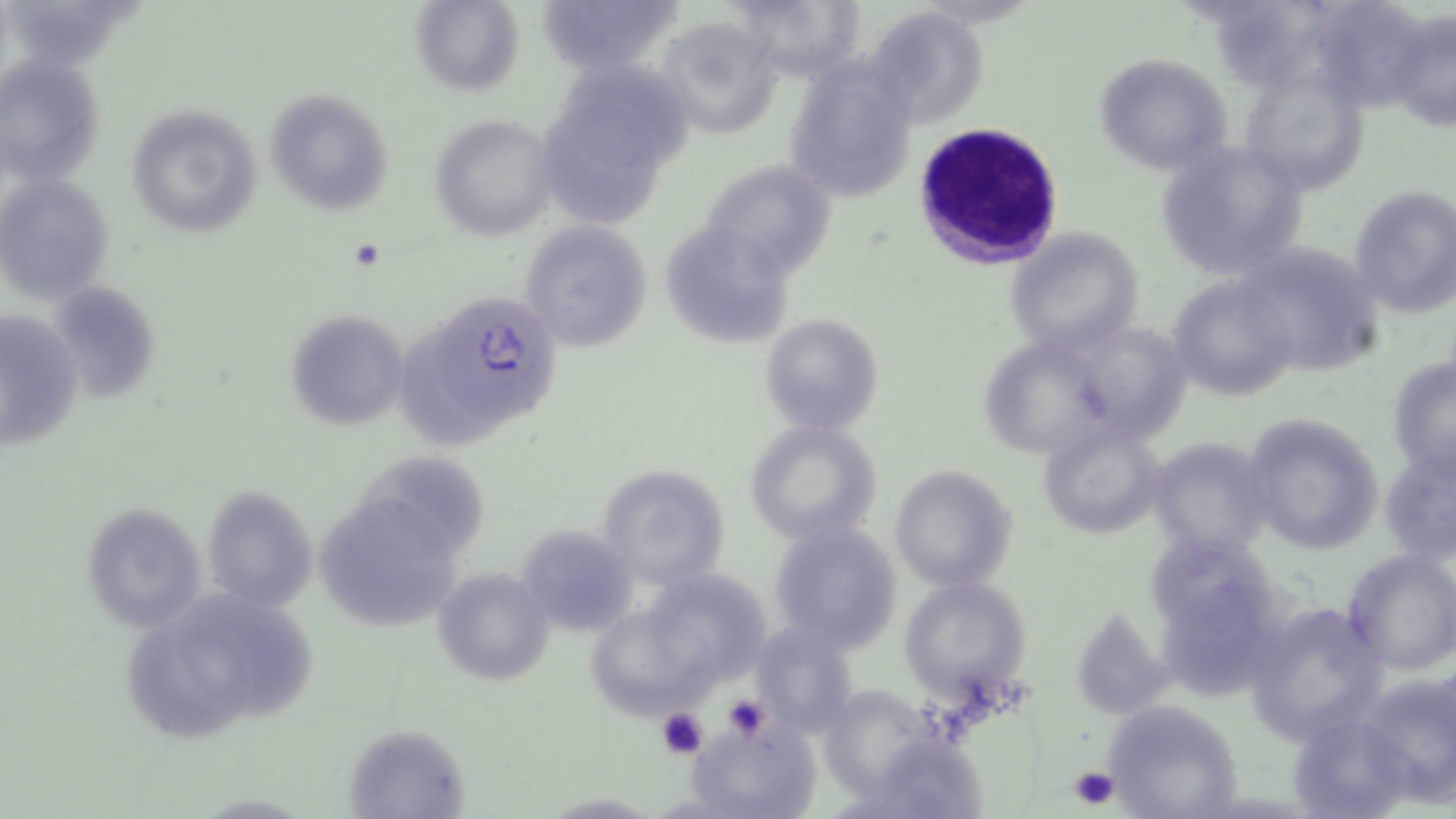
Approximate bounding boxes as (x1, y1, x2, y2) in pixels. Uninfected red blood cell locations: (408, 0, 524, 99), (724, 0, 866, 84), (533, 1, 681, 77), (1308, 1, 1435, 111), (866, 5, 989, 127), (1385, 13, 1456, 133), (655, 16, 782, 139), (1092, 52, 1235, 176), (0, 53, 107, 189), (782, 54, 920, 206), (574, 67, 694, 172), (1241, 67, 1370, 196), (262, 88, 397, 218), (125, 102, 262, 239), (562, 104, 664, 235), (429, 113, 560, 241), (1151, 140, 1311, 282), (697, 156, 839, 281), (1, 173, 116, 304), (1349, 184, 1456, 316), (517, 219, 655, 353), (1005, 225, 1145, 355), (666, 233, 812, 344), (1229, 242, 1384, 376), (1167, 272, 1300, 404), (47, 284, 159, 401), (1, 308, 83, 454), (285, 308, 411, 432), (760, 312, 885, 437), (1087, 328, 1209, 457), (979, 331, 1094, 454), (1387, 354, 1455, 480), (1242, 412, 1385, 553), (742, 418, 884, 547), (1037, 420, 1169, 538), (1146, 434, 1274, 560), (1378, 440, 1456, 567), (365, 450, 497, 556), (596, 463, 731, 593), (889, 464, 1018, 593), (201, 485, 317, 612), (326, 493, 461, 638), (78, 502, 206, 632), (767, 521, 905, 656), (515, 524, 637, 636), (1144, 534, 1268, 621), (1341, 547, 1456, 676), (658, 563, 768, 689), (432, 567, 556, 687), (901, 575, 1031, 702), (1174, 584, 1307, 697), (188, 593, 328, 737), (1242, 597, 1390, 745), (587, 607, 727, 727), (1074, 610, 1174, 708), (753, 619, 860, 738), (139, 629, 261, 748), (1358, 672, 1456, 802), (820, 680, 936, 791), (1103, 698, 1248, 817), (1286, 710, 1414, 819), (686, 714, 820, 819), (342, 722, 474, 817), (869, 733, 1014, 819). Platelet locations: (720, 694, 771, 741), (657, 708, 709, 758), (1068, 765, 1120, 811). White blood cell locations: (910, 122, 1065, 271). Plasmodium falciparum-infected red blood cell locations: (403, 287, 565, 443). Slide-level diagnosis: Plasmodium falciparum. One field of a larger specimen. Thin blood smear. Light microscopy. Captured at 1000x magnification. May-Grünwald-Giemsa-stained preparation. Image is 1456×819 pixels.